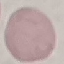
Summary:
  - Result: negative for malaria parasites
  - Image type: automatically extracted cell patch, resized to 64 × 64 pixels
  - Preparation: thin smear
  - Capture: smartphone camera at the microscope eyepiece
  - Stain: Giemsa